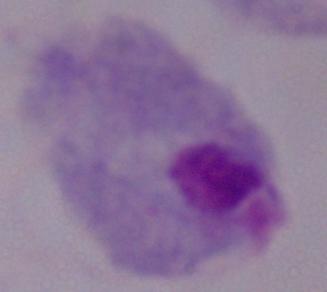 Captured at 1000x magnification. Micrograph. A trichomonad is seen.